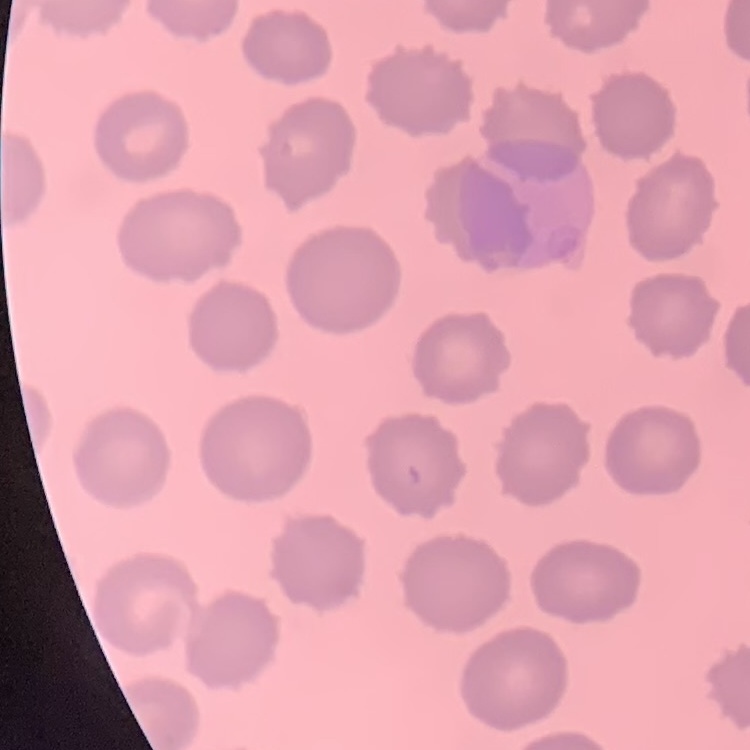
red blood cell morphology = no rouleaux formation
image type = one tile cut from a larger photomicrograph
preparation = thin blood smear
stain = Field's or Giemsa